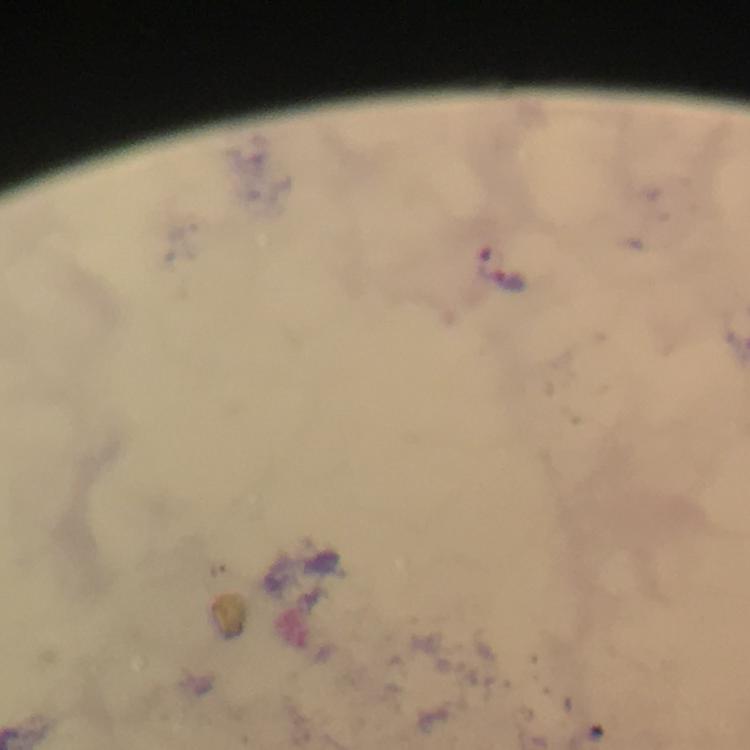

malaria parasite locations = approximate centers as {x, y} in pixels: {490, 260}, {511, 282}
cropped from = one field of view
magnification = 100x
image size = 750×750 pixels
context = from a malaria diagnostic workup
stain = Giemsa
preparation = thick smear
immersion oil = applied
capture = smartphone photograph through a microscope